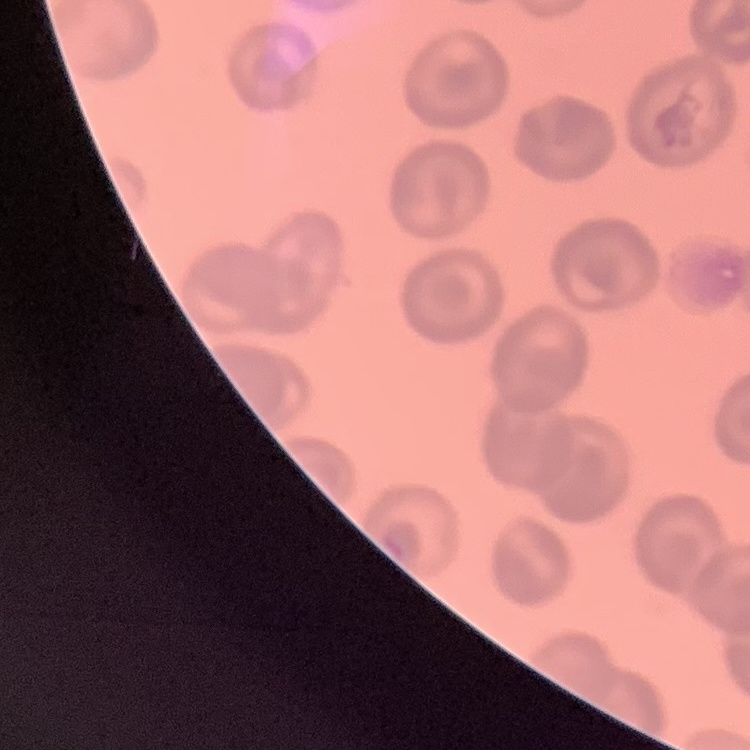
The erythrocytes show no rouleaux formation. Field's or Giemsa stain. One tile cut from a larger photomicrograph. Thin blood smear.